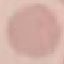
Summary:
  - Malaria status: uninfected
  - Image type: automatically extracted cell patch, resized to 64 × 64 pixels
  - Capture: smartphone through the microscope eyepiece
  - Preparation: thin blood film
  - Stain: Giemsa